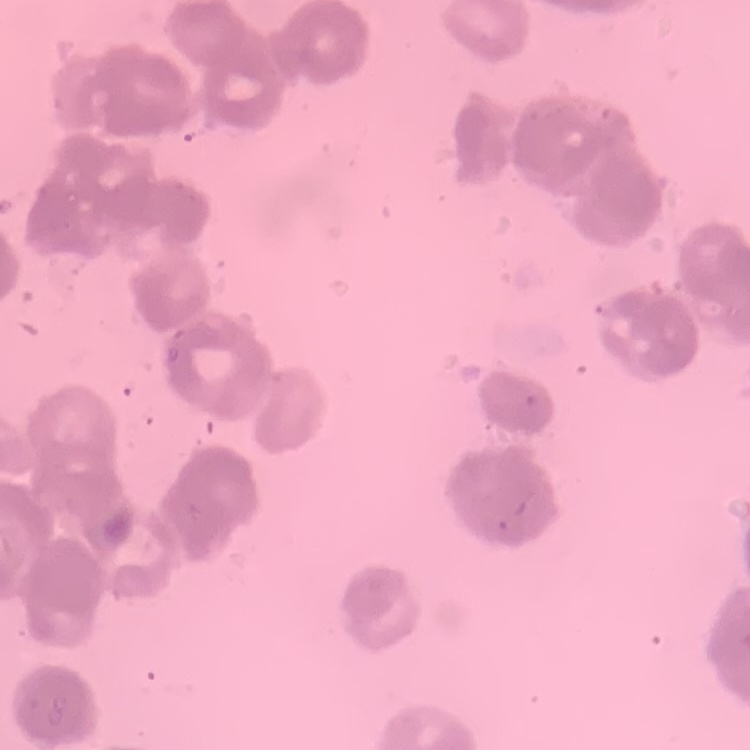

Summary:
  - Erythrocyte morphology: rouleaux formation
  - Stain: Field's or Giemsa
  - Preparation: thin peripheral smear
  - Image type: one tile cut from a larger photomicrograph